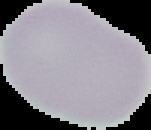

Summary:
  - Image type: segmented cell region with the area outside set to black
  - Image size: 151×130 pixels
  - Result: negative for malaria parasites
  - Preparation: thin blood film